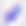

Photomicrograph. Captured at 400x magnification. Toxoplasma gondii is shown.